Describe the morphology of the red blood cells.
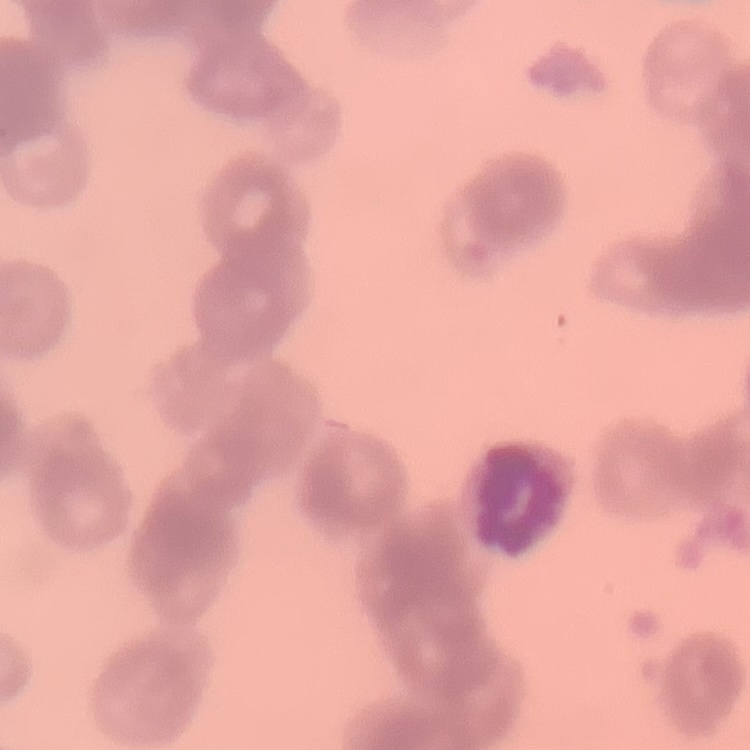

They show rouleaux formation.

stain = Field's or Giemsa
image type = square crop of a larger photomicrograph
preparation = thin blood film